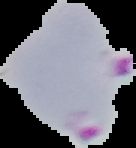
From a thin blood film. The area outside the segmented cell region is set to black. Result: malaria parasites detected. Image is 136×148 pixels.